State the preparation type.
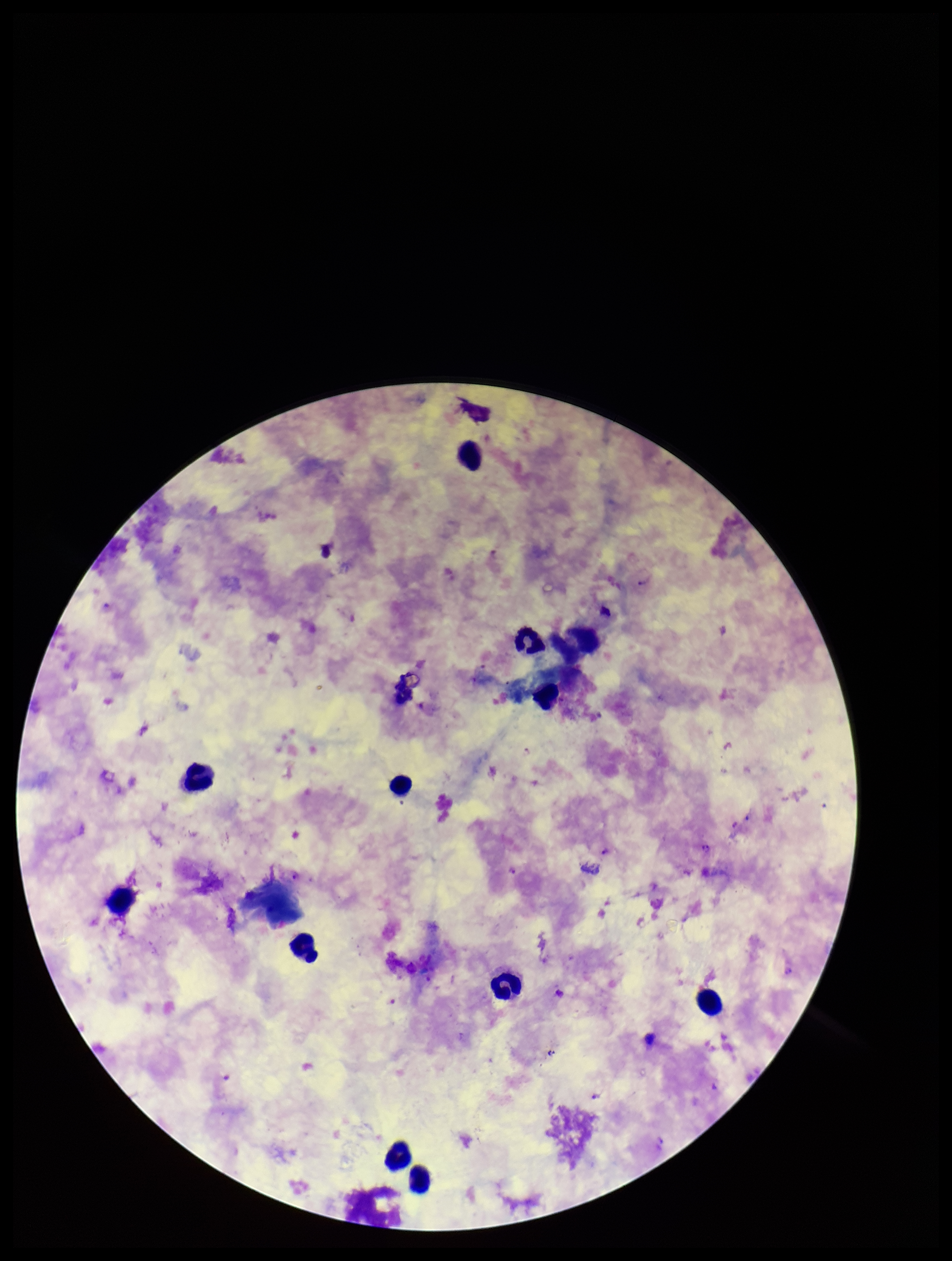
A thick smear.

leukocyte count = 12
image size = 952×1261 pixels
field of view = one from this slide
capture = smartphone photograph through the microscope eyepiece
stain = Giemsa
parasite count = 16
patient malaria status = infected
species reported for this patient = Plasmodium falciparum
Plasmodium parasites = seen